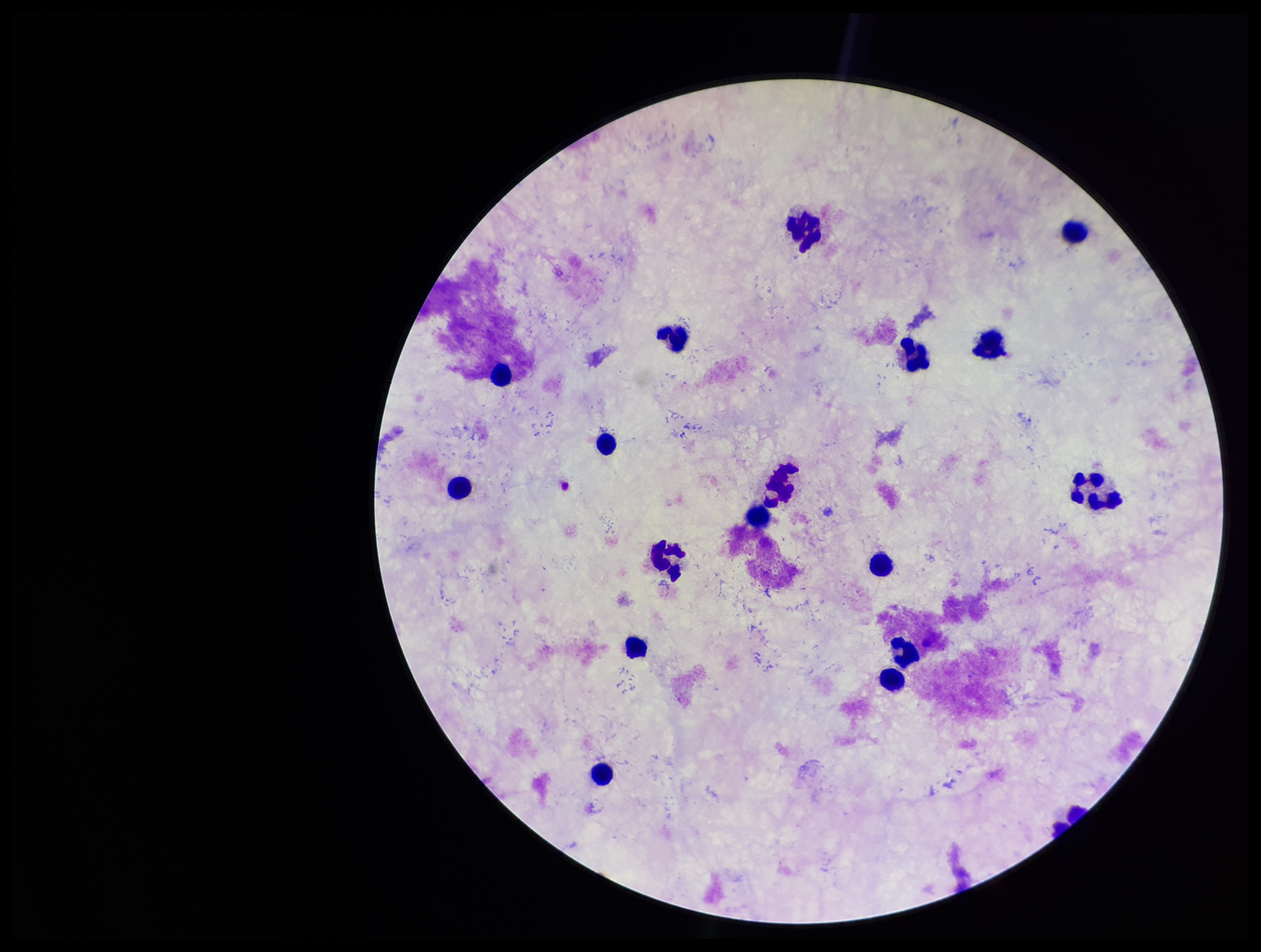
Summary:
  - Stain: Giemsa
  - Parasite count: 0
  - Preparation: thick blood smear
  - Capture: smartphone photograph through the microscope eyepiece
  - Patient malaria status: negative
  - Plasmodium parasites: none seen
  - Image size: 1261×952 pixels
  - Field of view: one from this slide
  - Leukocyte count: 16